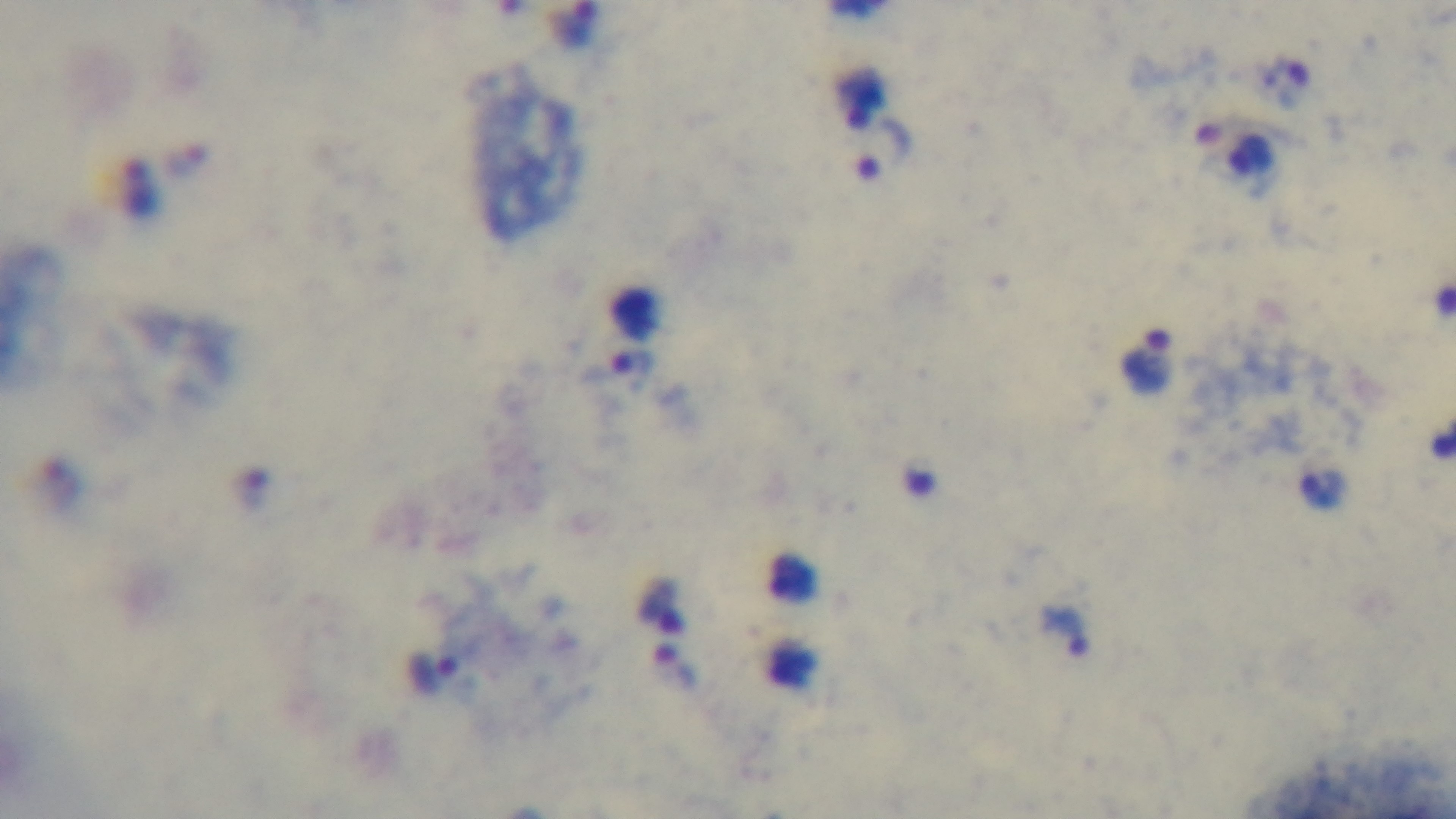
Summary:
  - Capture: mounted 4K digital camera
  - Malaria status: positive
  - Preparation: thick blood film
  - Stain: Giemsa
  - Objective: 100x oil immersion
  - Field of view: one from the slide
  - Modality: light microscopy